Identify the blood parasite species.
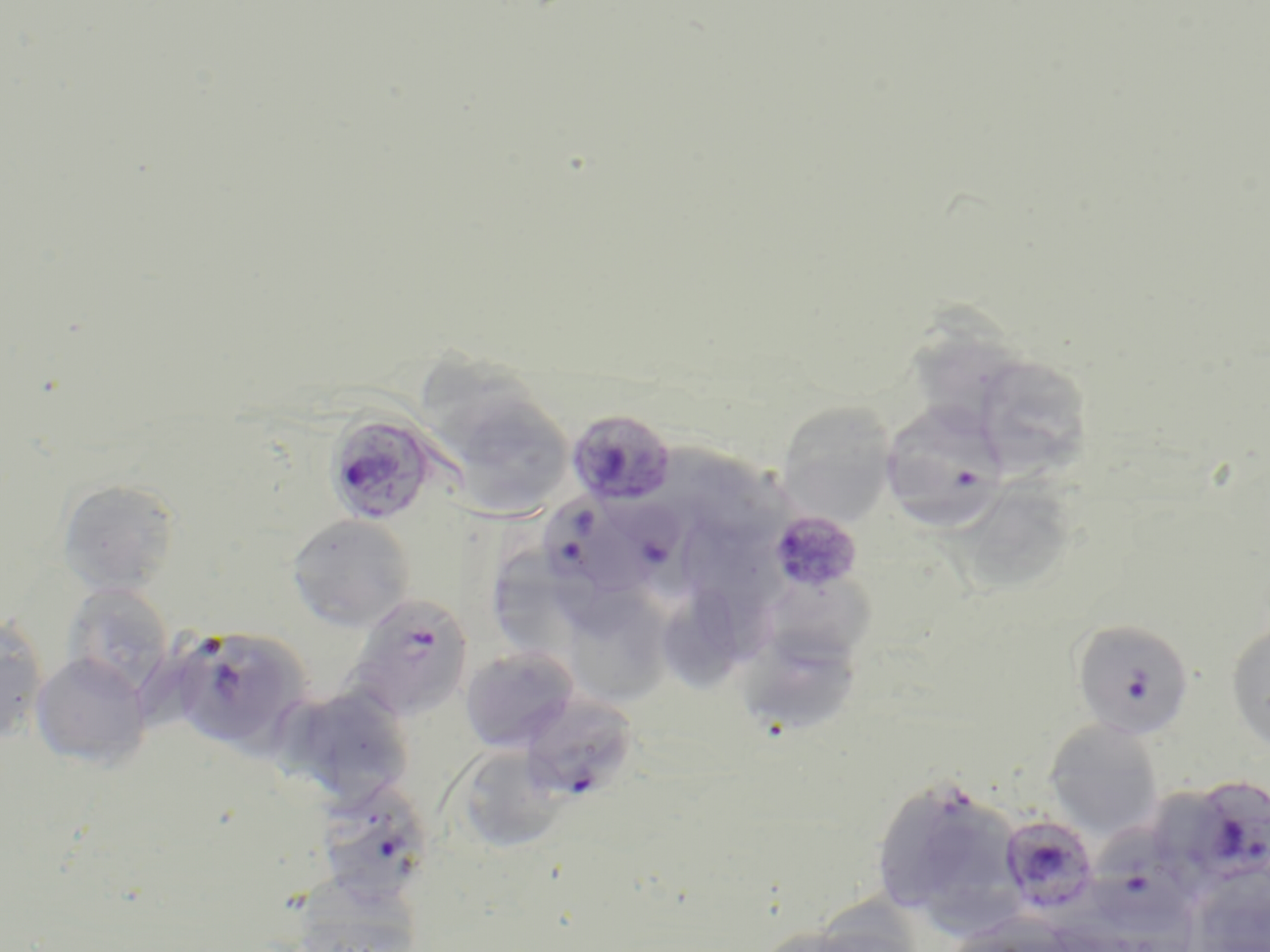
Plasmodium falciparum.

modality: optical microscopy
preparation: thin blood smear
field_of_view: single
magnification: 1000x
plasmodium_falciparum_infected_red_blood_cell_locations: 'approximate bounding boxes as (x1, y1, x2, y2) in pixels: (881, 402, 1010, 539), (566, 407, 677, 508), (324, 410, 441, 527), (633, 486, 721, 595), (541, 492, 648, 588), (769, 510, 864, 594), (347, 593, 474, 722), (1070, 619, 1194, 747), (168, 626, 309, 752), (519, 693, 638, 803), (1181, 775, 1270, 885), (312, 782, 435, 904), (999, 814, 1099, 915), (1087, 817, 1207, 939)'
uninfected_red_blood_cell_locations: 'approximate bounding boxes as (x1, y1, x2, y2) in pixels: (908, 310, 1023, 437), (419, 351, 554, 463), (971, 353, 1098, 477), (775, 401, 897, 525), (459, 405, 572, 517), (694, 449, 791, 549), (955, 477, 1070, 592), (57, 478, 182, 596), (287, 514, 416, 631), (688, 525, 779, 607), (494, 536, 578, 645), (760, 566, 874, 668), (62, 582, 174, 697), (664, 583, 747, 692), (560, 587, 674, 708), (0, 614, 49, 746), (1225, 618, 1270, 754), (748, 631, 857, 736), (459, 646, 579, 752), (30, 652, 151, 769), (272, 684, 416, 810), (1044, 719, 1165, 839), (452, 744, 566, 854), (885, 785, 970, 909), (927, 803, 1016, 943), (1189, 875, 1270, 952), (287, 876, 424, 951)'
stain: May-Grünwald-Giemsa
image_size: 1270×952 pixels